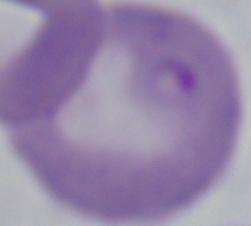
modality = photomicrograph
identification = Babesia
magnification = 1000x